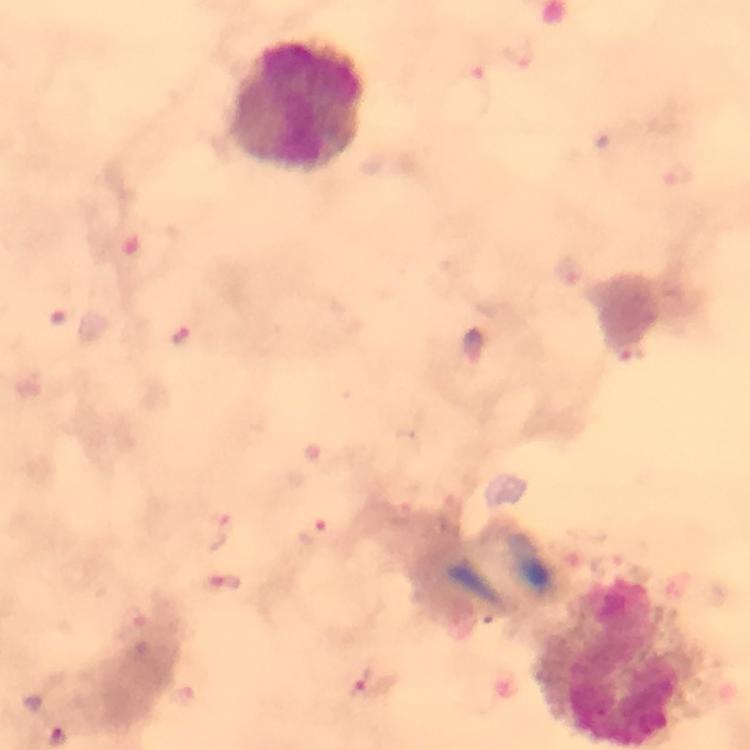

context = from a malaria diagnostic workup
leukocyte locations = approximate centers as [x, y] in pixels: [297, 105], [613, 664]
magnification = 100x
capture = smartphone mounted on the microscope
image size = 750×750 pixels
immersion oil = used
preparation = thick blood smear
cropped from = a single field of view
Plasmodium parasite locations = approximate centers as [x, y] in pixels: [179, 338], [634, 356], [314, 530], [224, 581], [361, 682]
stain = Giemsa